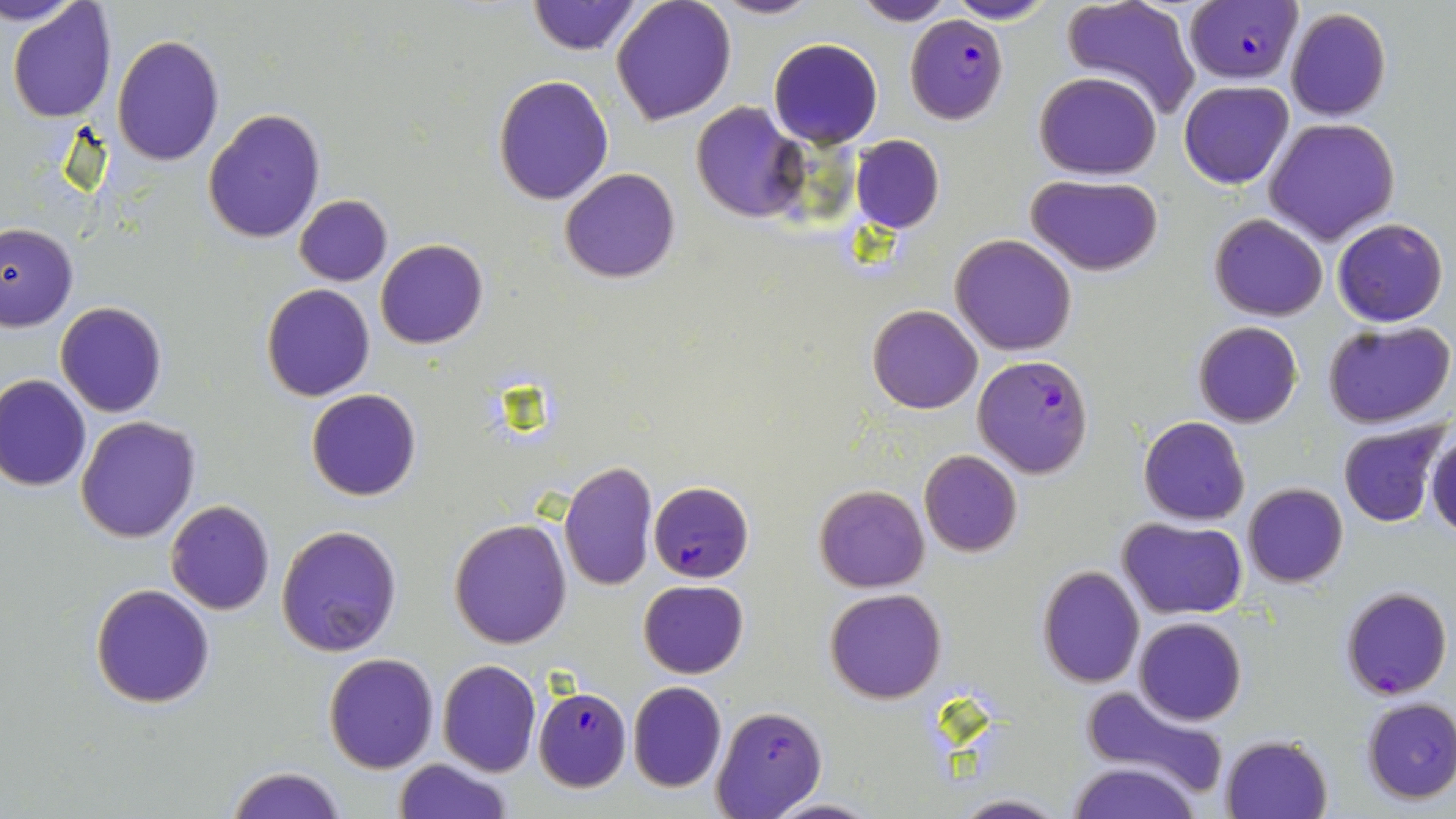 Approximate bounding boxes as (x1, y1, x2, y2) in pixels. Uninfected red blood cell locations: (3, 0, 84, 29), (611, 0, 737, 127), (712, 0, 820, 19), (851, 0, 953, 26), (946, 0, 1056, 24), (7, 1, 117, 120), (528, 1, 641, 55), (1058, 1, 1202, 120), (1284, 8, 1391, 123), (111, 35, 225, 167), (768, 38, 883, 149), (1033, 70, 1163, 179), (493, 76, 614, 205), (1179, 80, 1294, 190), (692, 102, 809, 221), (202, 108, 326, 245), (1265, 117, 1401, 244), (850, 134, 944, 233), (559, 167, 680, 284), (1027, 174, 1165, 275), (293, 195, 392, 285), (1209, 213, 1329, 321), (1332, 217, 1449, 327), (0, 222, 77, 331), (951, 235, 1076, 356), (376, 239, 488, 349), (263, 284, 375, 401), (56, 302, 168, 418), (866, 304, 982, 414), (1322, 320, 1455, 430), (1192, 321, 1303, 427), (0, 375, 92, 492), (306, 389, 423, 501), (76, 415, 200, 542), (1138, 416, 1250, 526), (1337, 421, 1448, 527), (1425, 429, 1456, 537), (918, 449, 1021, 558), (558, 461, 657, 591), (1242, 483, 1348, 588), (814, 484, 929, 592), (164, 499, 275, 614), (1118, 517, 1248, 619), (449, 518, 572, 649), (276, 524, 403, 657), (1037, 565, 1146, 688), (638, 579, 748, 678), (90, 584, 215, 708), (824, 588, 946, 703), (1134, 617, 1247, 725), (322, 653, 439, 773), (436, 659, 541, 777), (627, 681, 727, 793), (1080, 682, 1228, 792), (1361, 698, 1456, 804), (1219, 733, 1334, 819), (392, 757, 512, 819), (1067, 761, 1202, 819), (229, 766, 345, 819), (949, 794, 1070, 819), (762, 796, 881, 818). Plasmodium falciparum-infected red blood cell locations: (1177, 0, 1308, 82), (907, 16, 1008, 126), (973, 354, 1095, 478), (648, 480, 754, 584), (1341, 587, 1452, 699), (532, 686, 632, 792), (710, 705, 826, 817). Slide-level diagnosis: Plasmodium falciparum. Light microscopy. Image is 1456×819 pixels. Captured at 1000x magnification. Thin blood smear. May-Grünwald-Giemsa stain. One field of a larger specimen.